Assess this cell for malaria.
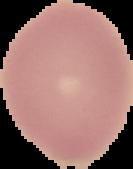
Uninfected.

image_type: segmented cell region on a black background
image_size: 133×169 pixels
preparation: thin blood smear